Locate every Plasmodium parasite.
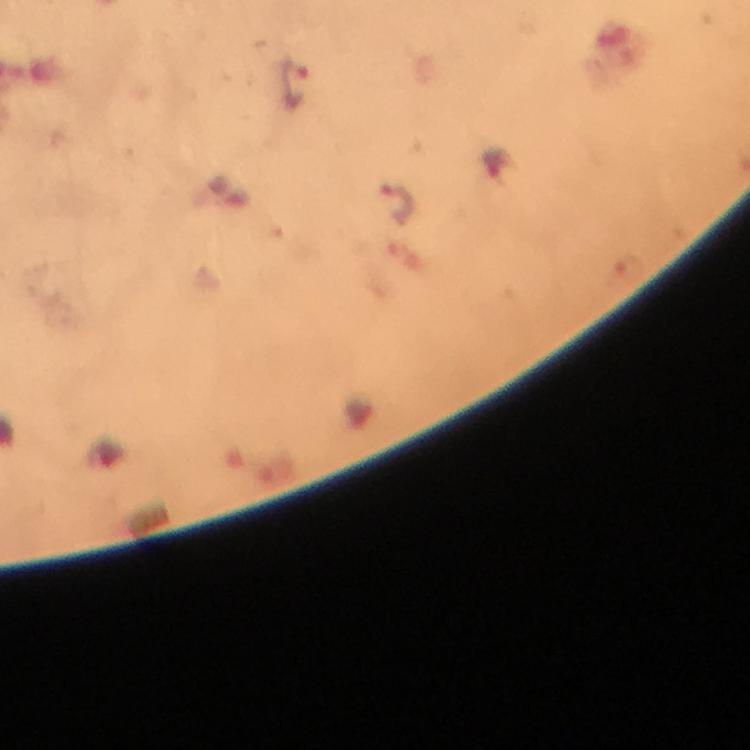

Approximate centers as [x, y] in pixels.
Plasmodium parasites: [294, 82], [396, 203].

Summary:
  - Stain: Giemsa
  - Immersion oil: applied
  - Magnification: 100x
  - Preparation: thick blood smear
  - Capture: smartphone mounted on the microscope
  - Image size: 750×750 pixels
  - Cropped from: one field of view
  - Context: from a diagnostic examination for malaria